State which cell type is depicted.
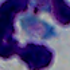
A leukocyte.

1000x magnification. Photomicrograph.